Outline each Plasmodium falciparum-infected red blood cell.
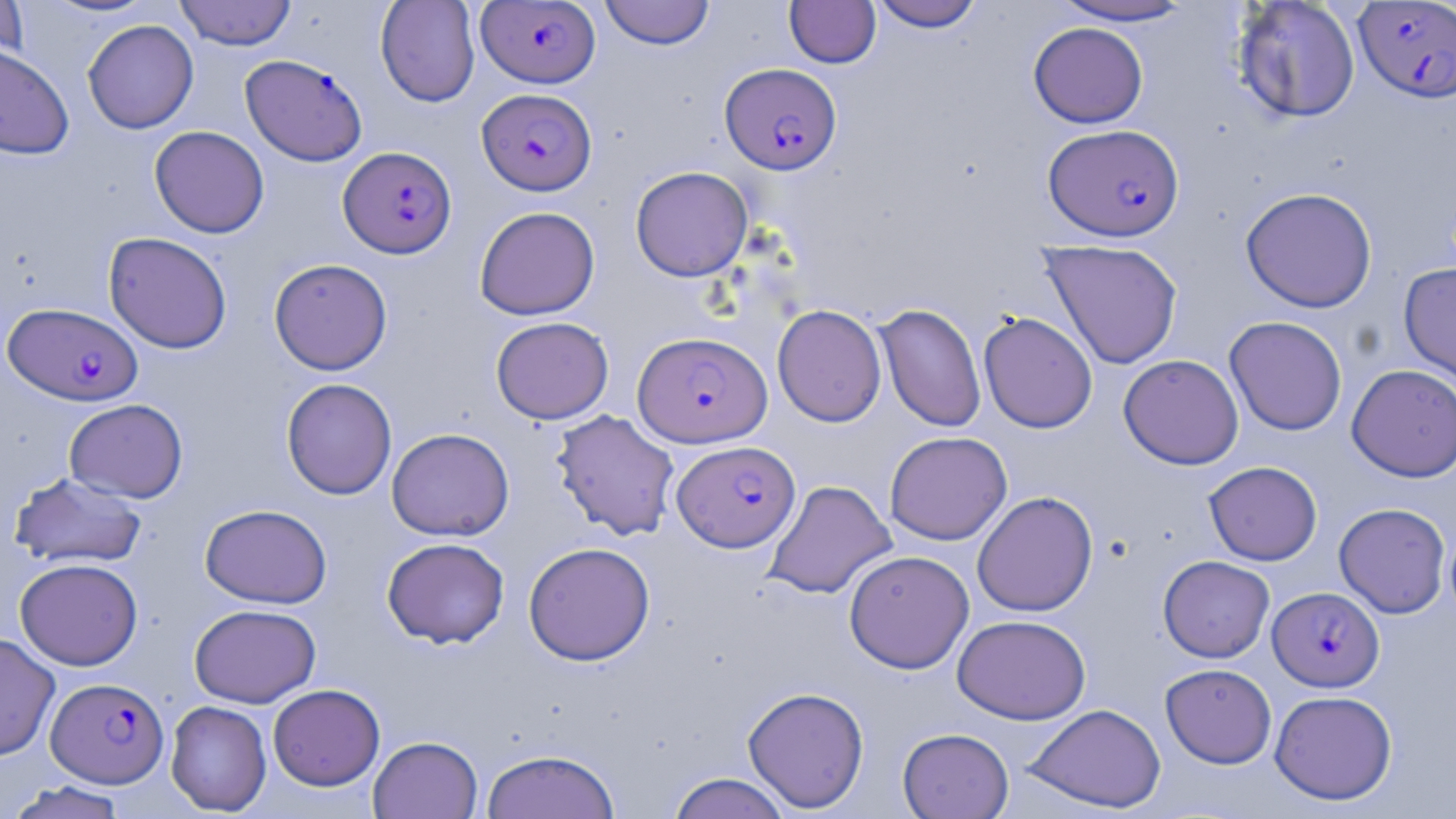

Approximate bounding boxes as [x1, y1, x2, y2] in pixels.
Plasmodium falciparum-infected red blood cells: [477, 1, 600, 87], [1353, 1, 1456, 103], [240, 54, 367, 167], [720, 63, 842, 175], [477, 88, 597, 195], [1043, 123, 1185, 241], [338, 146, 456, 258], [3, 302, 143, 406], [633, 331, 772, 448], [672, 440, 800, 552], [1268, 587, 1384, 691], [46, 677, 168, 787].

Summary:
  - Uninfected red blood cell locations: [0, 0, 30, 70], [40, 0, 160, 18], [174, 0, 296, 49], [375, 0, 480, 108], [600, 0, 715, 49], [784, 1, 881, 68], [870, 1, 985, 32], [1049, 1, 1197, 26], [1231, 1, 1361, 124], [82, 19, 199, 134], [1028, 22, 1148, 128], [0, 44, 75, 160], [149, 125, 269, 238], [630, 165, 753, 282], [1240, 187, 1378, 313], [474, 206, 600, 320], [103, 232, 233, 353], [1040, 239, 1183, 369], [269, 258, 392, 375], [1398, 262, 1456, 389], [874, 303, 986, 432], [772, 304, 887, 427], [978, 312, 1098, 433], [1224, 315, 1347, 436], [490, 316, 614, 424], [1118, 354, 1244, 470], [1347, 364, 1456, 482], [281, 378, 397, 499], [64, 399, 188, 503], [550, 409, 680, 540], [386, 427, 514, 541], [884, 431, 1013, 545], [1204, 461, 1322, 566], [10, 471, 148, 570], [763, 479, 897, 599], [972, 490, 1098, 617], [1334, 502, 1451, 618], [199, 503, 332, 608], [381, 537, 510, 648], [523, 541, 656, 666], [844, 550, 974, 673], [1158, 555, 1275, 662], [15, 557, 143, 670], [189, 603, 320, 708], [952, 614, 1091, 725], [0, 632, 60, 760], [1160, 663, 1277, 768], [268, 683, 385, 790], [742, 686, 870, 812], [1270, 690, 1397, 805], [166, 700, 272, 815], [1024, 703, 1166, 814], [897, 727, 1014, 818], [368, 735, 482, 819], [480, 748, 621, 819], [666, 772, 793, 819], [5, 780, 130, 819]
  - Slide-level diagnosis: Plasmodium falciparum
  - Modality: optical microscopy
  - Stain: May-Grünwald-Giemsa
  - Image size: 1456×819 pixels
  - Field of view: single
  - Magnification: 1000x
  - Preparation: thin blood film